Locate every blood parasite and identify its species.
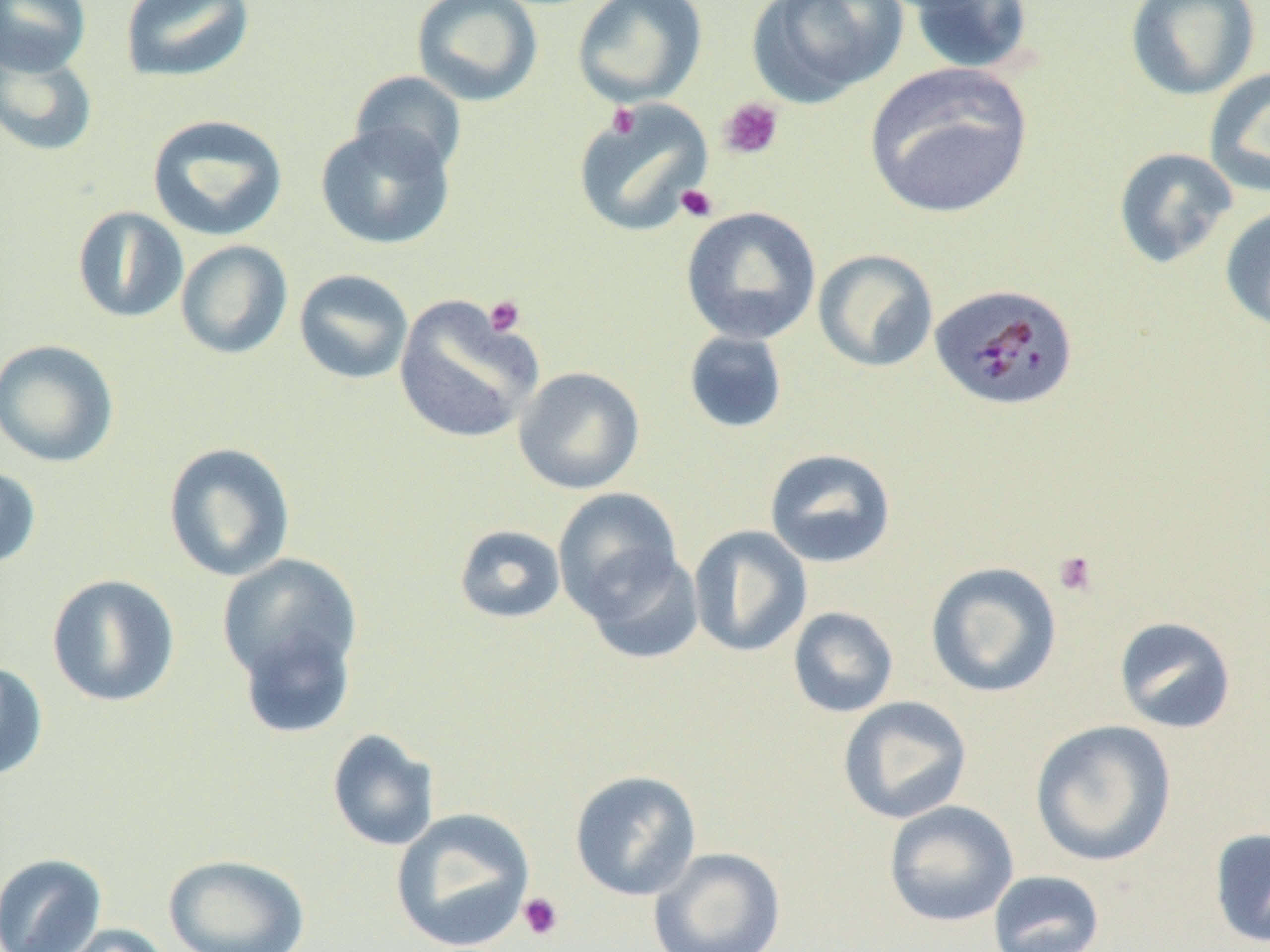
Approximate bounding boxes as (x1,y1)-(x2,y2) corner pairs in pixels.
Plasmodium malariae-infected red blood cells: (930,283)-(1080,411).
No Plasmodium falciparum, Plasmodium ovale, Plasmodium vivax, Babesia divergens, or Trypanosoma brucei observed.

slide-level diagnosis = Plasmodium malariae
magnification = 1000x
field of view = single
uninfected red blood cell locations = approximate bounding boxes as (x1,y1)-(x2,y2) corner pairs in pixels: (1,0)-(91,77), (412,0)-(543,107), (572,0)-(707,106), (747,0)-(907,106), (904,0)-(1036,75), (1125,0)-(1261,101), (120,1)-(255,84), (0,47)-(99,157), (864,61)-(1035,219), (1203,67)-(1270,198), (349,71)-(467,176), (571,100)-(712,236), (146,114)-(288,241), (315,123)-(456,250), (1113,147)-(1238,269), (1219,204)-(1270,334), (71,206)-(189,324), (681,206)-(821,344), (175,240)-(293,360), (813,249)-(938,373), (293,269)-(414,385), (393,296)-(542,445), (682,330)-(789,435), (0,338)-(120,468), (513,366)-(644,495), (163,442)-(296,582), (763,448)-(897,568), (0,464)-(42,570), (552,488)-(683,617), (454,525)-(566,624), (688,525)-(813,658), (580,546)-(705,664), (217,553)-(362,697), (925,561)-(1063,698), (46,573)-(181,708), (787,606)-(899,718), (1113,616)-(1237,734), (236,620)-(358,740), (0,659)-(48,782), (837,696)-(973,824), (1029,719)-(1177,866), (326,729)-(440,852), (569,769)-(702,901), (883,800)-(1019,928), (389,806)-(536,951), (1209,828)-(1270,947), (648,847)-(786,952), (0,852)-(108,952), (164,853)-(310,952), (987,869)-(1105,952), (44,923)-(174,952)
platelet locations = approximate bounding boxes as (x1,y1)-(x2,y2) corner pairs in pixels: (718,97)-(784,160), (607,103)-(640,139), (675,184)-(719,222), (483,295)-(526,337), (1052,550)-(1099,598), (517,892)-(565,941)
image size = 1270×952 pixels
modality = light microscopy
preparation = thin blood film